Comment on the morphology of the erythrocytes.
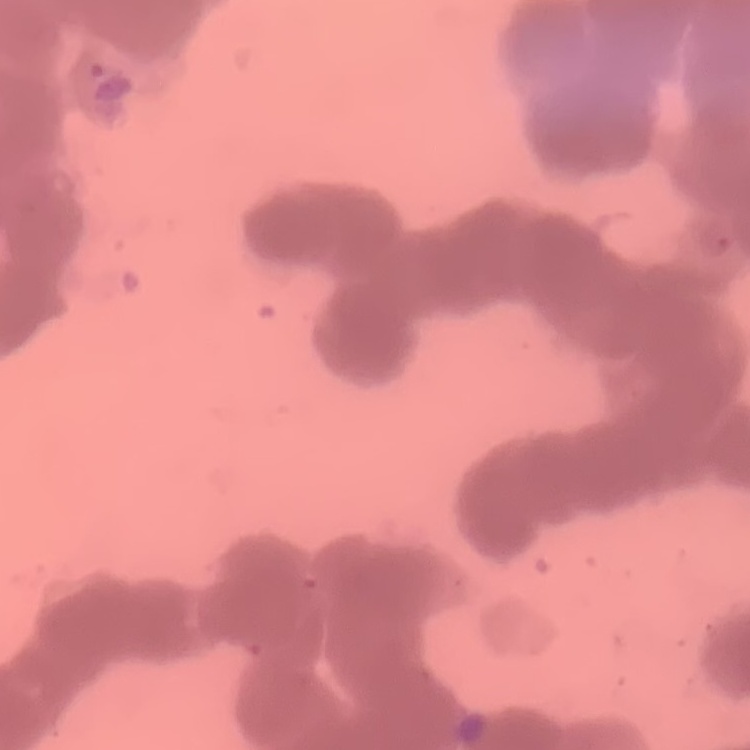

They show rouleaux formation.

Field's or Giemsa stain. Thin blood film. Square crop of a larger photomicrograph.